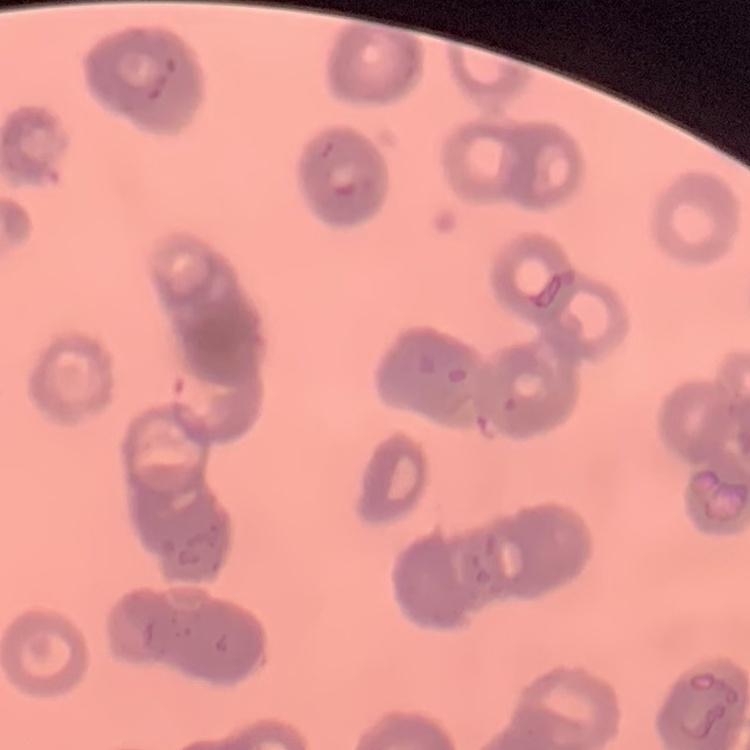
erythrocyte morphology = rouleaux formation
stain = Field's or Giemsa
preparation = thin peripheral smear
image type = square crop of a larger photomicrograph